Assess for Plasmodium parasites.
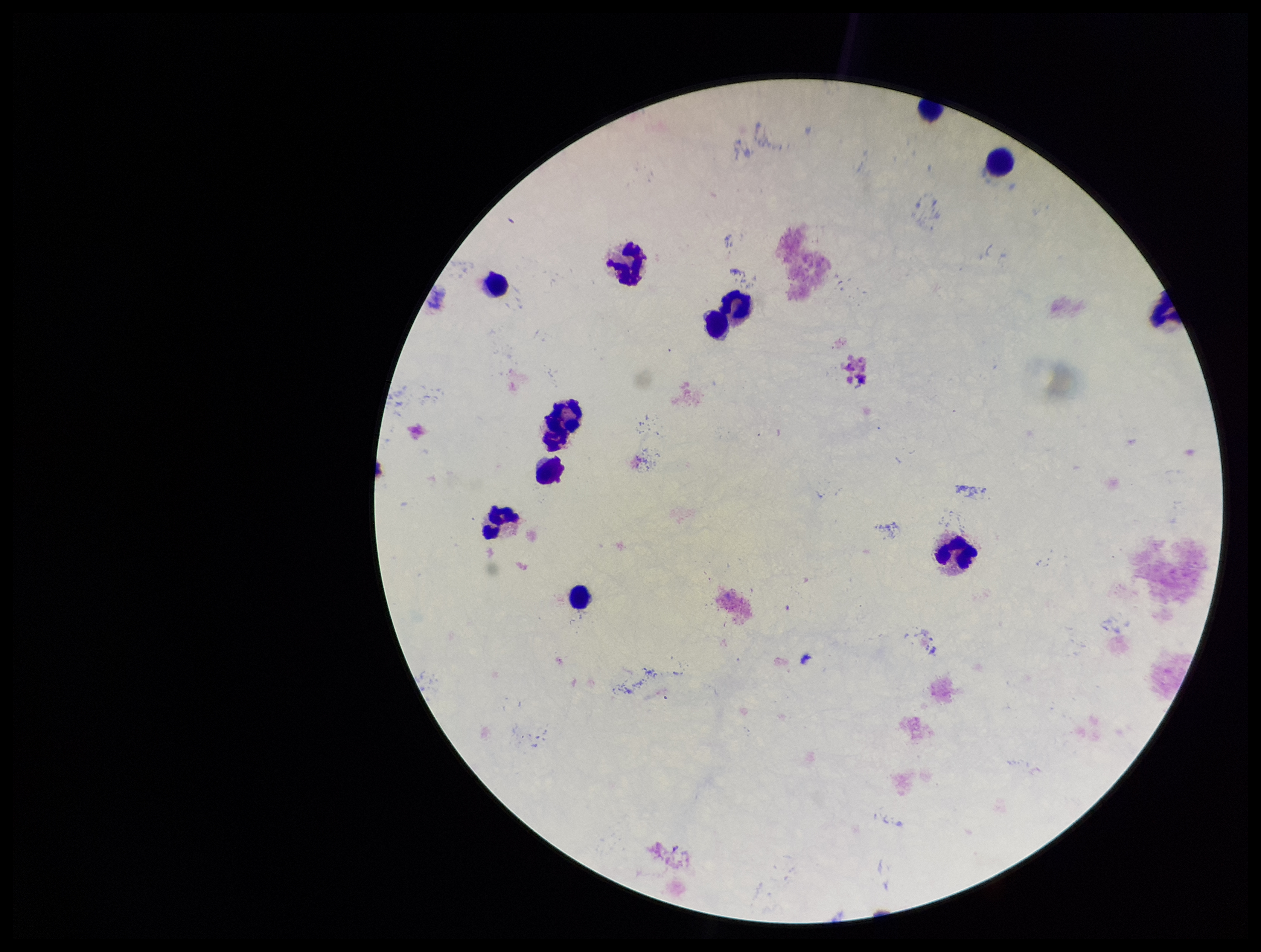
None detected.

Summary:
  - Capture: smartphone photograph through the microscope eyepiece
  - Image size: 1261×952 pixels
  - Field of view: single
  - Leukocyte count: 12
  - Parasite count: 0
  - Preparation: thick blood smear
  - Patient malaria status: negative
  - Stain: Giemsa